Give the position of every Plasmodium parasite.
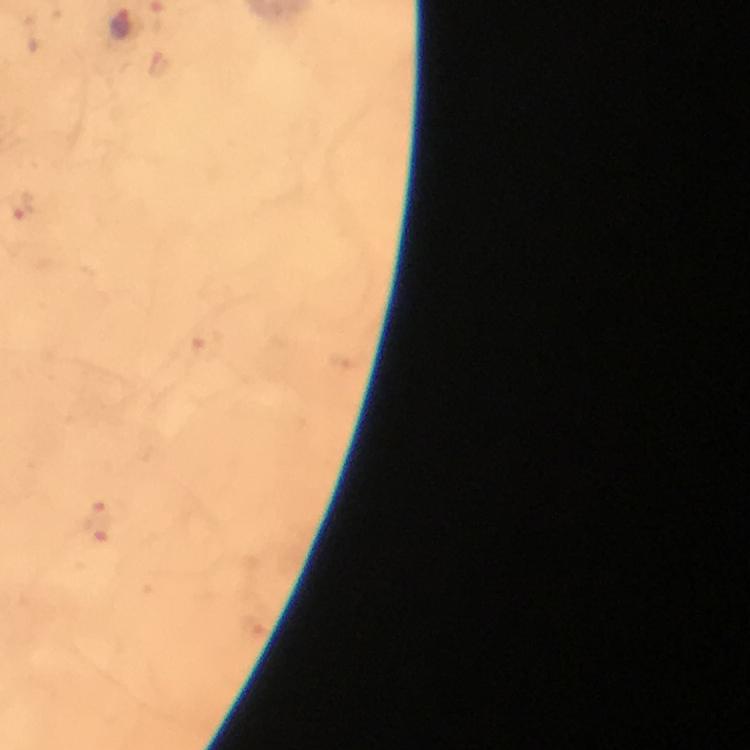
Approximate centers as (x, y) in pixels.
Plasmodium parasites: (121, 23), (23, 205), (101, 529).

immersion oil = applied
preparation = thick blood film
stain = Giemsa
cropped from = a single field of view
context = from a diagnostic examination for malaria
capture = smartphone photograph through a microscope
image size = 750×750 pixels
magnification = 100x